Locate every blood parasite and identify its species.
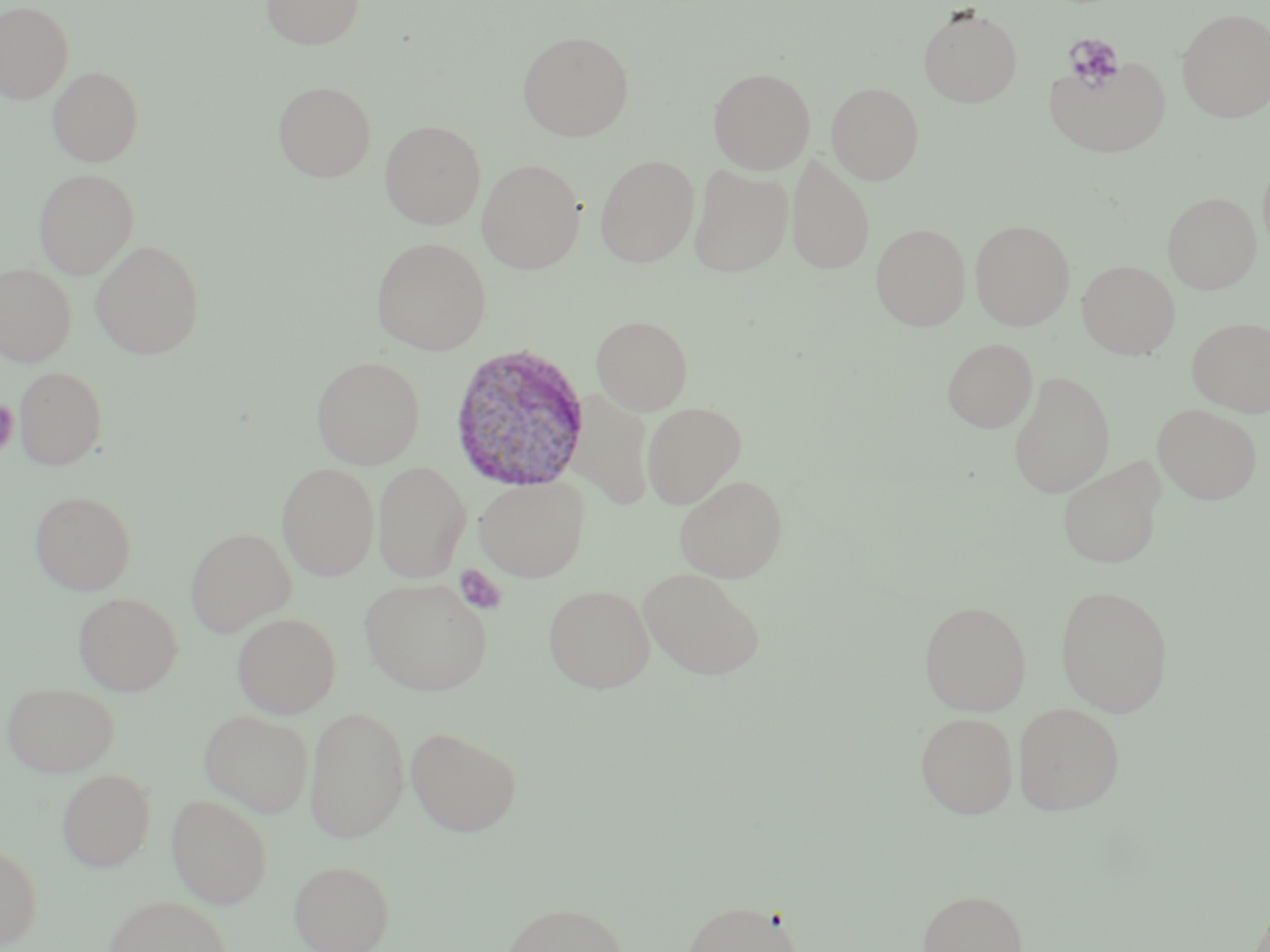

Approximate bounding boxes as [x1, y1, x2, y2] in pixels.
Plasmodium vivax-infected red blood cells: [447, 342, 590, 493].
No Plasmodium falciparum, Plasmodium ovale, Plasmodium malariae, Babesia divergens, or Trypanosoma brucei observed.

Uninfected red blood cell locations: [261, 0, 364, 49], [0, 1, 74, 104], [917, 6, 1023, 108], [1177, 7, 1270, 122], [517, 30, 634, 141], [1044, 54, 1172, 158], [48, 66, 144, 166], [708, 67, 815, 174], [273, 81, 377, 182], [826, 81, 924, 184], [379, 120, 486, 229], [786, 152, 875, 274], [594, 154, 699, 267], [477, 159, 585, 273], [688, 164, 794, 277], [34, 168, 139, 279], [1163, 192, 1261, 293], [970, 220, 1075, 330], [871, 223, 970, 332], [371, 236, 491, 355], [90, 239, 205, 359], [1077, 260, 1180, 359], [0, 262, 77, 367], [591, 315, 693, 415], [1187, 317, 1270, 416], [942, 337, 1037, 432], [311, 356, 425, 469], [15, 367, 107, 470], [1008, 370, 1115, 498], [567, 389, 654, 510], [641, 401, 747, 508], [1153, 403, 1263, 504], [1057, 457, 1166, 569], [372, 461, 472, 582], [277, 462, 380, 580], [674, 473, 788, 582], [474, 475, 590, 581], [29, 490, 137, 595], [185, 528, 296, 636], [638, 567, 766, 680], [360, 577, 494, 695], [543, 584, 655, 693], [1054, 584, 1173, 717], [73, 592, 183, 695], [919, 600, 1031, 715], [233, 612, 341, 718], [3, 683, 119, 777], [1013, 702, 1125, 815], [304, 704, 410, 843], [199, 709, 315, 818], [915, 711, 1019, 818], [406, 725, 522, 836], [57, 768, 155, 872], [167, 793, 272, 909], [0, 841, 42, 948], [289, 860, 394, 952], [918, 888, 1028, 952], [103, 895, 232, 952], [680, 899, 805, 952], [501, 900, 629, 952]. Platelet locations: [1064, 33, 1125, 90], [0, 399, 20, 457], [454, 564, 507, 615]. Slide-level diagnosis: Plasmodium vivax. Image is 1270×952 pixels. Captured at 1000x magnification. Light microscopy. Single field of view. May-Grünwald-Giemsa stain. Thin blood film.